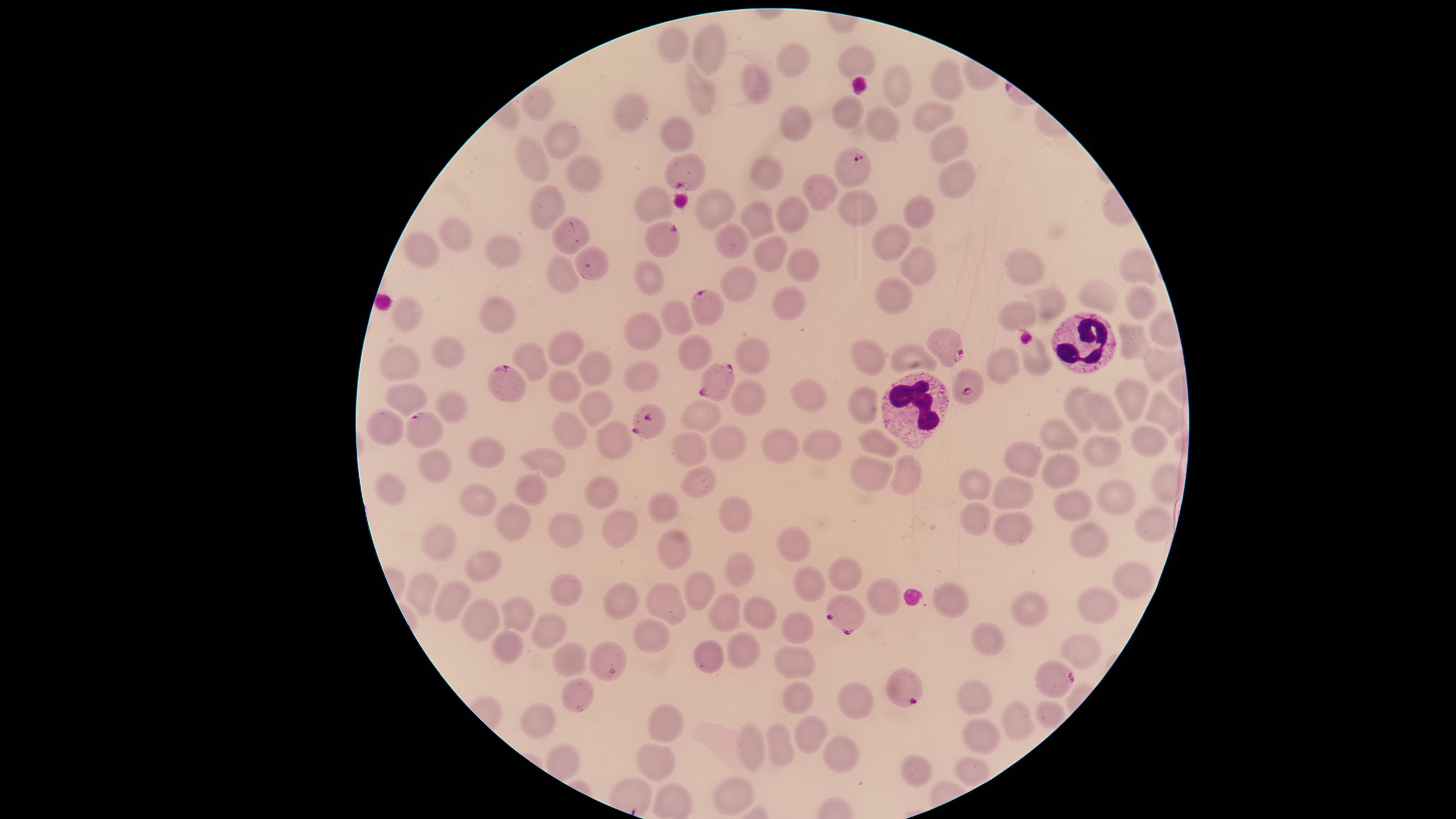
Approximate marker points, in pixels from the top-left corner.
Summary:
  - Uninfected red blood cells: (x=677, y=45), (x=709, y=53), (x=797, y=57), (x=861, y=60), (x=949, y=83), (x=757, y=84), (x=897, y=84), (x=694, y=94), (x=540, y=100), (x=847, y=112), (x=625, y=113), (x=931, y=115), (x=878, y=119), (x=792, y=123), (x=675, y=134), (x=557, y=137), (x=942, y=142), (x=531, y=158), (x=582, y=167), (x=772, y=171), (x=958, y=176), (x=819, y=190), (x=653, y=203), (x=710, y=205), (x=551, y=209), (x=849, y=209), (x=917, y=210), (x=793, y=213), (x=757, y=219), (x=456, y=235), (x=730, y=238), (x=890, y=244), (x=770, y=252), (x=412, y=254), (x=506, y=254), (x=802, y=261), (x=1025, y=261), (x=916, y=262), (x=1136, y=266), (x=565, y=273), (x=650, y=273), (x=738, y=284), (x=895, y=299), (x=1092, y=299), (x=781, y=302), (x=1134, y=302), (x=1052, y=306), (x=403, y=314), (x=499, y=315), (x=1014, y=317), (x=679, y=318), (x=645, y=330), (x=1161, y=332), (x=1125, y=339), (x=689, y=346), (x=451, y=349), (x=564, y=350), (x=751, y=353), (x=532, y=358), (x=868, y=358), (x=910, y=358), (x=1035, y=360), (x=999, y=364), (x=1160, y=365), (x=401, y=366), (x=593, y=366), (x=647, y=375), (x=559, y=387), (x=803, y=392), (x=746, y=395), (x=1133, y=396), (x=407, y=399), (x=862, y=405), (x=1075, y=405), (x=453, y=406), (x=597, y=406), (x=1164, y=412), (x=707, y=418), (x=1109, y=419), (x=383, y=427), (x=566, y=430), (x=620, y=432), (x=1060, y=435), (x=725, y=438), (x=1146, y=440), (x=826, y=441), (x=880, y=442), (x=782, y=444), (x=689, y=446), (x=482, y=450), (x=1098, y=456), (x=550, y=461), (x=1029, y=461), (x=866, y=468), (x=1061, y=469), (x=440, y=470), (x=909, y=476), (x=699, y=480), (x=968, y=483), (x=1162, y=483), (x=598, y=486), (x=390, y=488), (x=532, y=488), (x=999, y=491), (x=1112, y=496), (x=476, y=501), (x=1073, y=504), (x=661, y=508), (x=975, y=512), (x=736, y=515), (x=515, y=520), (x=619, y=520), (x=1150, y=523), (x=1007, y=526), (x=567, y=535), (x=1094, y=535), (x=803, y=544), (x=438, y=545), (x=680, y=548), (x=731, y=563), (x=483, y=566), (x=840, y=573), (x=1129, y=577), (x=699, y=587), (x=811, y=587), (x=570, y=590), (x=949, y=592), (x=423, y=595), (x=670, y=595), (x=888, y=599), (x=457, y=602), (x=621, y=602), (x=1095, y=604), (x=758, y=612), (x=725, y=613), (x=1033, y=613), (x=521, y=616), (x=480, y=622), (x=801, y=627), (x=550, y=632), (x=652, y=637), (x=984, y=641), (x=508, y=643), (x=1083, y=648), (x=740, y=650), (x=703, y=655), (x=567, y=659), (x=800, y=663), (x=795, y=696), (x=851, y=697), (x=573, y=699), (x=963, y=701), (x=1055, y=711), (x=534, y=713), (x=1021, y=721), (x=667, y=723), (x=804, y=733), (x=978, y=736), (x=779, y=746), (x=754, y=748), (x=833, y=750), (x=563, y=759), (x=662, y=759), (x=967, y=769), (x=919, y=772), (x=735, y=797)
  - Parasitized red blood cells: (x=683, y=171), (x=664, y=233), (x=708, y=307), (x=947, y=344), (x=714, y=377), (x=972, y=386), (x=513, y=388), (x=650, y=422), (x=425, y=426), (x=847, y=618), (x=1057, y=674), (x=902, y=686)
  - White blood cells: (x=1083, y=336), (x=917, y=410)
  - Species: Plasmodium falciparum
  - Stain: Giemsa
  - Image size: 1456×819 pixels
  - Visible region: circular
  - Field of view: single
  - Presence: malaria parasites detected
  - Preparation: thin smear of blood
  - Capture: smartphone photograph through the microscope eyepiece